Classify this cell by malaria status.
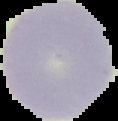

It is uninfected.

Summary:
  - Preparation: thin blood smear
  - Image type: cell region segmented out of the field of view; surrounding area masked to black
  - Image size: 118×121 pixels